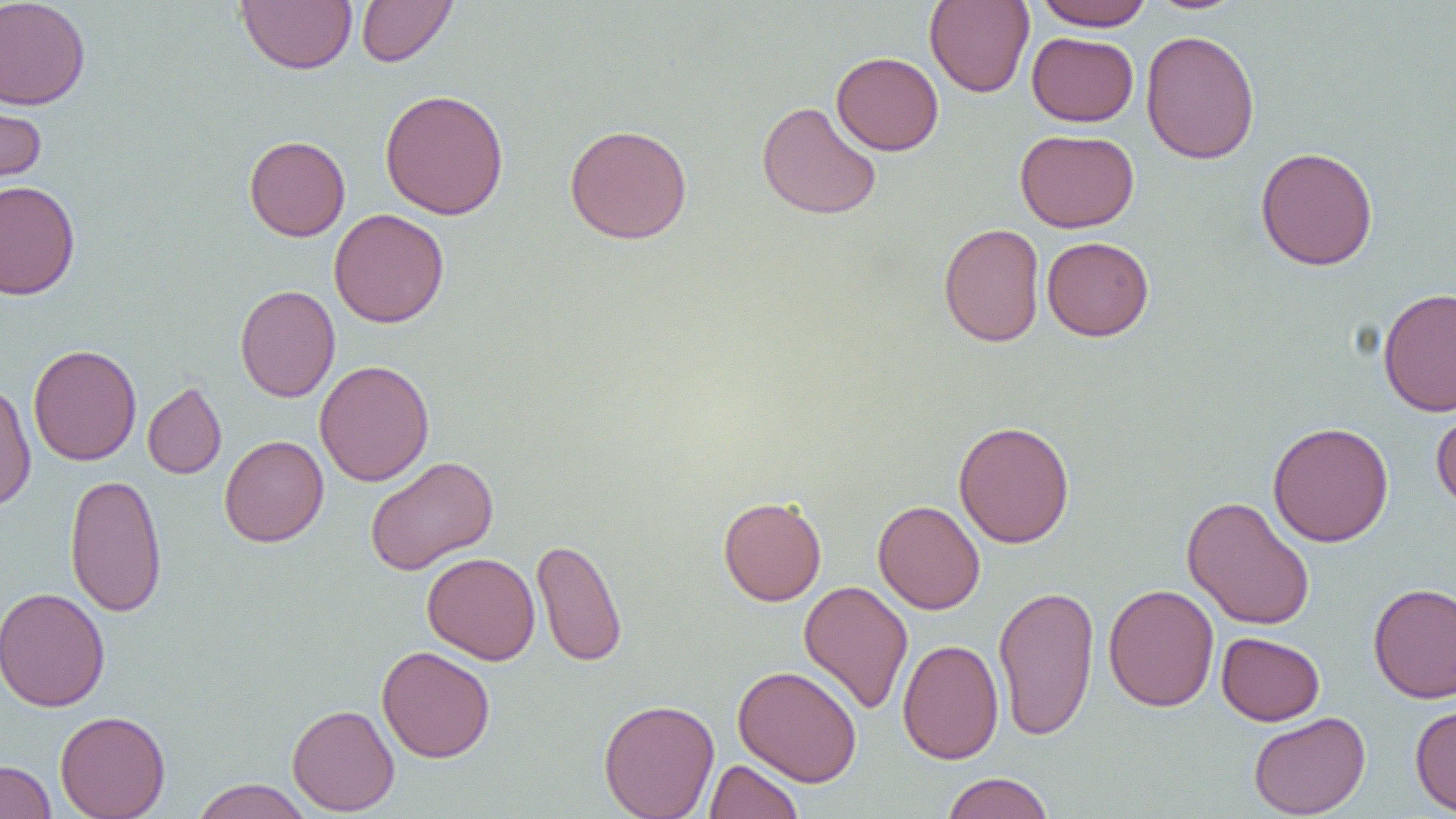
Approximate bounding boxes as (x1, y1, x2, y2) in pixels. Uninfected red blood cell locations: (0, 0, 91, 110), (236, 0, 357, 74), (356, 0, 458, 67), (924, 0, 1034, 98), (1033, 0, 1155, 31), (1145, 0, 1249, 15), (1140, 30, 1260, 165), (1027, 32, 1138, 126), (831, 52, 944, 156), (380, 89, 509, 220), (0, 94, 48, 197), (756, 100, 882, 220), (565, 124, 692, 244), (1015, 129, 1139, 233), (244, 135, 351, 241), (1255, 147, 1379, 271), (0, 180, 81, 300), (329, 208, 449, 328), (938, 222, 1045, 347), (1042, 236, 1154, 341), (235, 285, 339, 402), (1377, 287, 1456, 416), (28, 344, 142, 465), (314, 359, 435, 486), (0, 381, 36, 511), (142, 381, 227, 479), (1431, 402, 1456, 515), (953, 420, 1075, 548), (1268, 421, 1394, 546), (219, 434, 329, 547), (364, 456, 498, 575), (64, 473, 168, 617), (718, 496, 827, 606), (1181, 496, 1316, 631), (873, 500, 985, 614), (531, 537, 628, 667), (422, 552, 540, 664), (799, 580, 913, 715), (1368, 582, 1456, 703), (1103, 583, 1219, 712), (993, 584, 1099, 742), (0, 586, 110, 711), (1216, 632, 1324, 725), (897, 638, 1004, 764), (376, 645, 495, 763), (733, 665, 863, 787), (598, 698, 720, 819), (287, 704, 400, 816), (1410, 705, 1456, 816), (55, 710, 171, 818), (1248, 711, 1370, 819), (704, 759, 803, 819), (0, 760, 56, 819), (940, 772, 1055, 818), (189, 779, 316, 819). Slide-level diagnosis: no evidence of blood parasites. Single field of view. Image is 1456×819 pixels. Thin blood smear. 1000x magnification. Light microscopy.